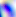
Summary:
  - Magnification: 400x
  - Identification: Toxoplasma gondii
  - Modality: micrograph